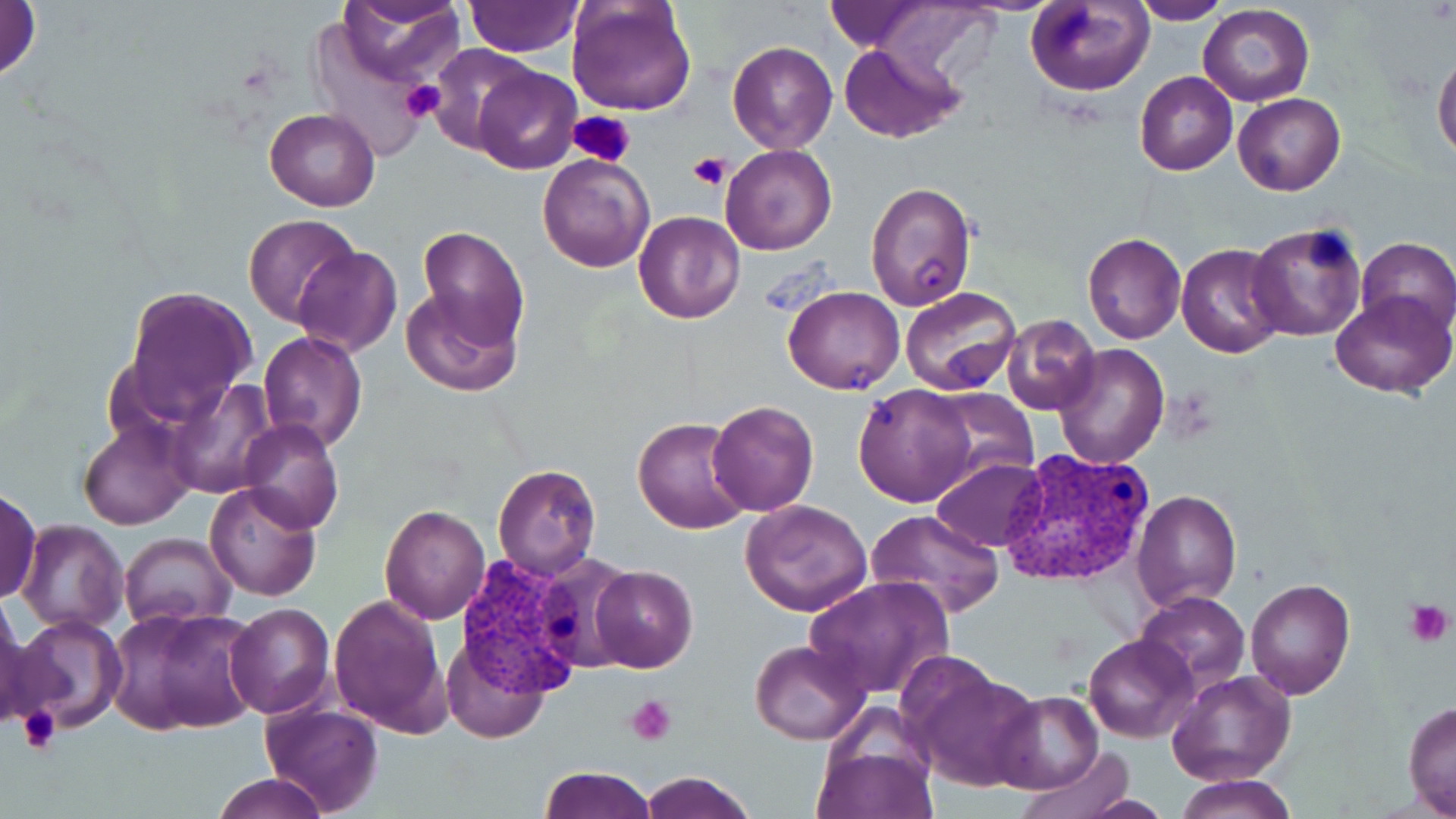
{
  "slide_level_diagnosis": "Plasmodium vivax",
  "image_size": "1456×819 pixels",
  "field_of_view": "one of a larger specimen",
  "uninfected_red_blood_cell_locations": "approximate bounding boxes as named x1/y1/x2/y2 corners in pixels: (x1=0, y1=0, x2=42, y2=87), (x1=333, y1=0, x2=465, y2=84), (x1=461, y1=0, x2=583, y2=55), (x1=567, y1=0, x2=697, y2=116), (x1=860, y1=0, x2=1000, y2=81), (x1=1130, y1=0, x2=1228, y2=24), (x1=1026, y1=1, x2=1153, y2=96), (x1=1198, y1=6, x2=1315, y2=107), (x1=727, y1=39, x2=838, y2=154), (x1=838, y1=41, x2=966, y2=143), (x1=427, y1=43, x2=540, y2=155), (x1=1432, y1=47, x2=1456, y2=165), (x1=472, y1=63, x2=581, y2=174), (x1=1135, y1=71, x2=1238, y2=176), (x1=1233, y1=92, x2=1345, y2=197), (x1=265, y1=107, x2=380, y2=211), (x1=720, y1=144, x2=836, y2=255), (x1=537, y1=154, x2=654, y2=272), (x1=864, y1=179, x2=975, y2=311), (x1=633, y1=210, x2=746, y2=325), (x1=243, y1=213, x2=361, y2=328), (x1=1245, y1=223, x2=1367, y2=342), (x1=414, y1=224, x2=529, y2=353), (x1=1082, y1=232, x2=1186, y2=343), (x1=1355, y1=236, x2=1456, y2=337), (x1=1176, y1=242, x2=1288, y2=360), (x1=293, y1=244, x2=401, y2=358), (x1=120, y1=284, x2=257, y2=423), (x1=399, y1=285, x2=520, y2=395), (x1=784, y1=285, x2=905, y2=395), (x1=899, y1=287, x2=1021, y2=395), (x1=1330, y1=290, x2=1454, y2=397), (x1=1002, y1=313, x2=1102, y2=416), (x1=258, y1=331, x2=367, y2=452), (x1=1052, y1=344, x2=1169, y2=470), (x1=167, y1=378, x2=278, y2=498), (x1=853, y1=382, x2=978, y2=507), (x1=928, y1=388, x2=1039, y2=486), (x1=707, y1=400, x2=818, y2=516), (x1=633, y1=416, x2=754, y2=535), (x1=79, y1=418, x2=197, y2=531), (x1=238, y1=420, x2=344, y2=535), (x1=930, y1=456, x2=1049, y2=553), (x1=492, y1=463, x2=601, y2=580), (x1=205, y1=482, x2=321, y2=602), (x1=0, y1=485, x2=44, y2=605), (x1=1132, y1=489, x2=1242, y2=612), (x1=741, y1=500, x2=873, y2=618), (x1=379, y1=503, x2=489, y2=624), (x1=865, y1=507, x2=1004, y2=618), (x1=17, y1=519, x2=128, y2=635), (x1=120, y1=533, x2=236, y2=629), (x1=588, y1=565, x2=698, y2=673), (x1=806, y1=575, x2=954, y2=699), (x1=1244, y1=576, x2=1356, y2=700), (x1=1135, y1=591, x2=1250, y2=692), (x1=329, y1=593, x2=451, y2=737), (x1=0, y1=602, x2=32, y2=729), (x1=224, y1=603, x2=335, y2=719), (x1=109, y1=604, x2=261, y2=739), (x1=7, y1=613, x2=127, y2=735), (x1=1083, y1=633, x2=1198, y2=742), (x1=750, y1=638, x2=871, y2=745), (x1=442, y1=639, x2=552, y2=744), (x1=902, y1=663, x2=1045, y2=794), (x1=1166, y1=671, x2=1295, y2=788), (x1=992, y1=691, x2=1105, y2=794), (x1=1402, y1=700, x2=1456, y2=817), (x1=257, y1=702, x2=385, y2=818), (x1=811, y1=708, x2=940, y2=819), (x1=1016, y1=748, x2=1137, y2=819), (x1=538, y1=766, x2=656, y2=819), (x1=637, y1=770, x2=757, y2=819), (x1=212, y1=773, x2=332, y2=819), (x1=1175, y1=775, x2=1297, y2=819)",
  "modality": "light microscopy",
  "platelet_locations": "approximate bounding boxes as named x1/y1/x2/y2 corners in pixels: (x1=399, y1=78, x2=446, y2=125), (x1=569, y1=109, x2=637, y2=169), (x1=688, y1=151, x2=732, y2=188), (x1=1403, y1=598, x2=1452, y2=648), (x1=626, y1=695, x2=677, y2=747), (x1=18, y1=704, x2=63, y2=756)",
  "preparation": "thin blood smear",
  "stain": "May-Grünwald-Giemsa",
  "magnification": "1000x",
  "plasmodium_vivax_infected_red_blood_cell_locations": "approximate bounding boxes as named x1/y1/x2/y2 corners in pixels: (x1=999, y1=447, x2=1159, y2=588), (x1=455, y1=555, x2=587, y2=700)"
}